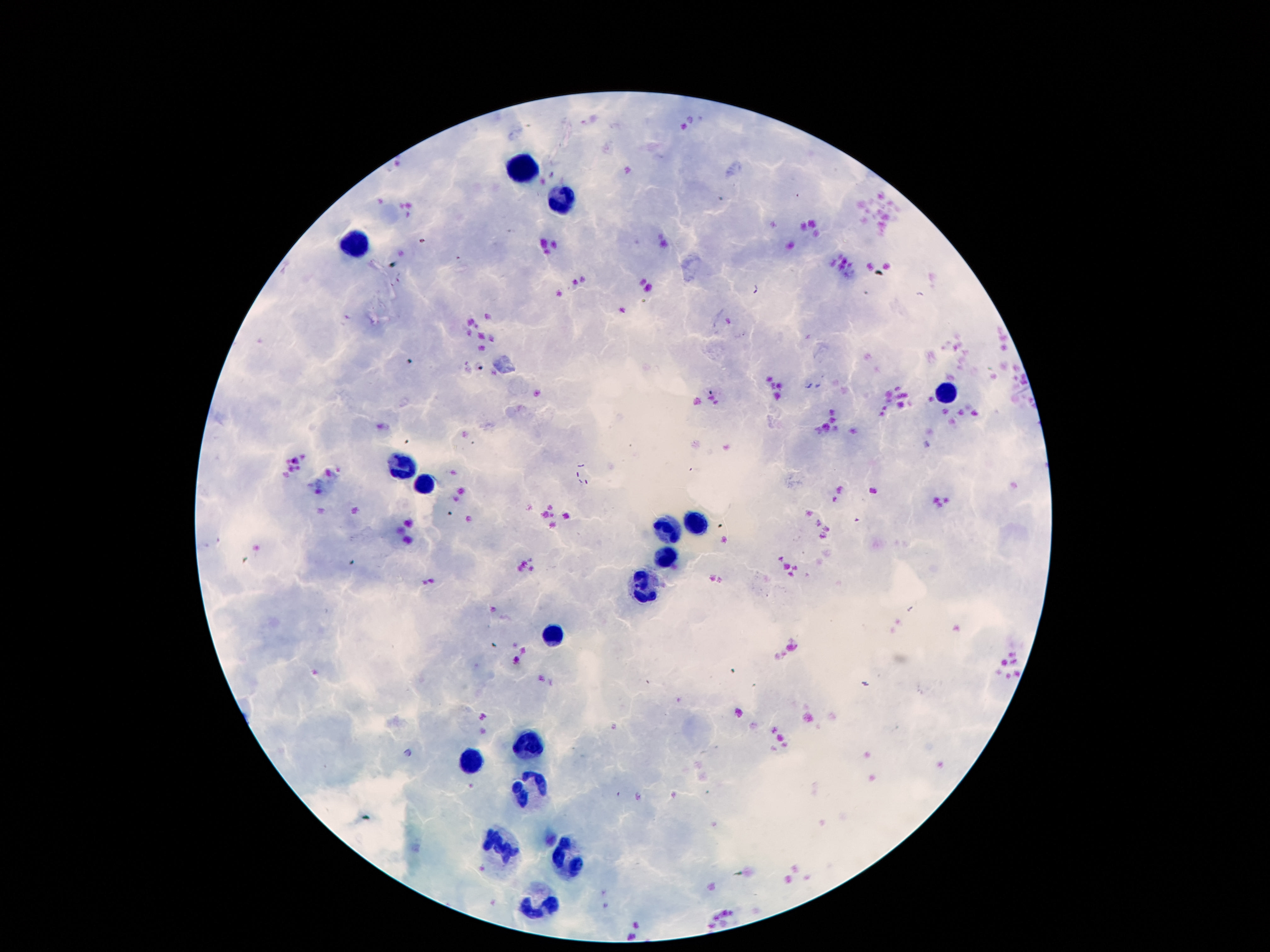
Approximate centers as (x, y) in pixels. Leukocyte locations: (517, 167), (560, 201), (353, 241), (949, 392), (400, 470), (427, 490), (699, 521), (662, 528), (666, 560), (640, 588), (558, 636), (525, 747), (470, 762), (531, 788), (492, 844), (560, 863), (539, 898). Image is 1270×952 pixels. Patient malaria status: uninfected. 100x magnification. Photographed through the microscope eyepiece with a smartphone camera. Single field of view. Giemsa stain. Thick blood smear.